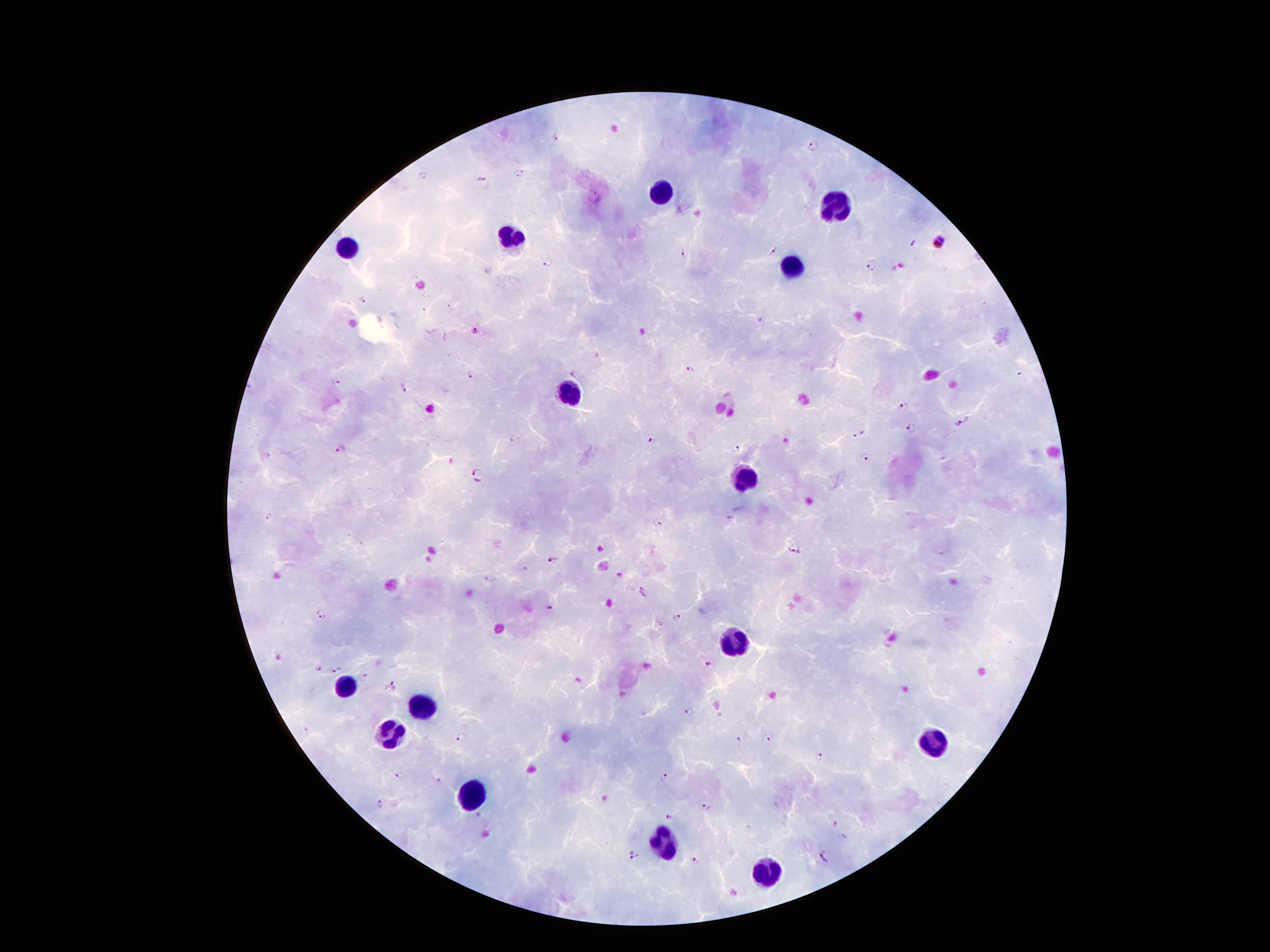
Approximate centers as {x, y} in pixels.
Summary:
  - Leukocyte locations: {665, 192}, {838, 212}, {512, 235}, {349, 248}, {792, 268}, {568, 393}, {744, 477}, {733, 640}, {346, 688}, {420, 708}, {392, 736}, {935, 744}, {471, 792}, {667, 848}, {766, 866}
  - Plasmodium parasite locations: {555, 136}, {812, 146}, {521, 170}, {424, 175}, {482, 179}, {939, 241}, {914, 242}, {774, 252}, {683, 256}, {547, 263}, {872, 265}, {362, 300}, {764, 321}, {476, 332}, {691, 369}, {470, 374}, {573, 374}, {334, 381}, {401, 387}, {905, 408}, {959, 424}, {910, 427}, {858, 435}, {516, 440}, {652, 440}, {342, 448}, {736, 449}, {268, 455}, {865, 456}, {476, 474}, {269, 517}, {659, 522}, {794, 551}, {554, 558}, {491, 578}, {645, 592}, {549, 609}, {321, 614}, {678, 616}, {709, 663}, {316, 668}, {336, 669}, {363, 677}, {389, 686}, {687, 711}, {462, 738}, {770, 738}, {739, 740}, {820, 757}, {397, 778}, {665, 779}, {439, 780}, {381, 805}, {707, 807}, {669, 817}, {835, 824}, {635, 855}, {825, 857}, {693, 860}
  - Capture: smartphone camera through the microscope eyepiece
  - Image size: 1270×952 pixels
  - Field of view: single
  - Patient malaria status: positive for Plasmodium falciparum
  - Magnification: 100x
  - Preparation: thick blood film
  - Stain: Giemsa